Classify this cell by malaria status.
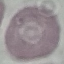
It is uninfected.

capture = smartphone camera at the microscope eyepiece
stain = Giemsa
image type = automatically extracted cell patch, resized to 64 × 64 pixels
preparation = thin blood film